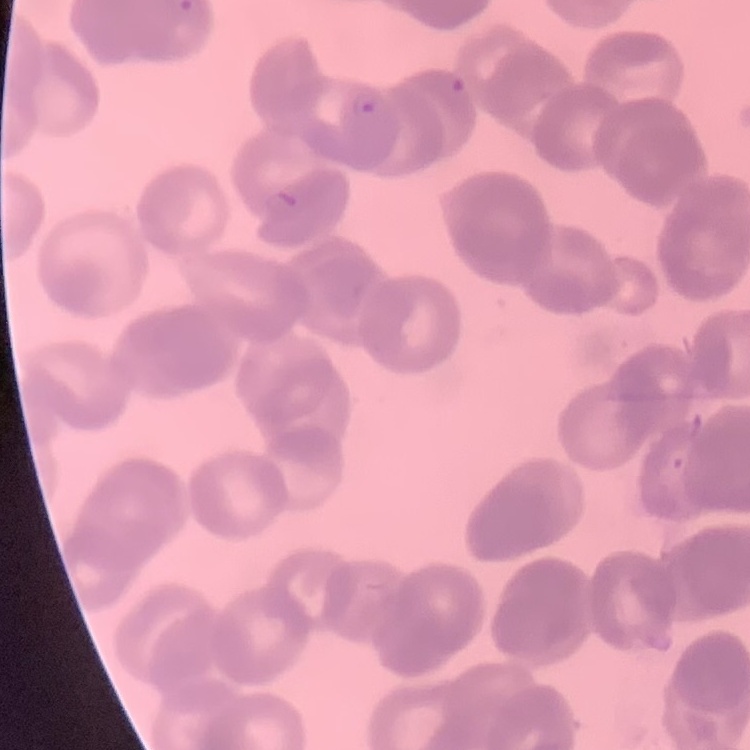

red blood cell morphology = rouleaux formation
stain = Field's or Giemsa
image type = one tile cut from a larger photomicrograph
preparation = thin peripheral smear